Give the extent of all Plasmodium falciparum-infected red blood cells.
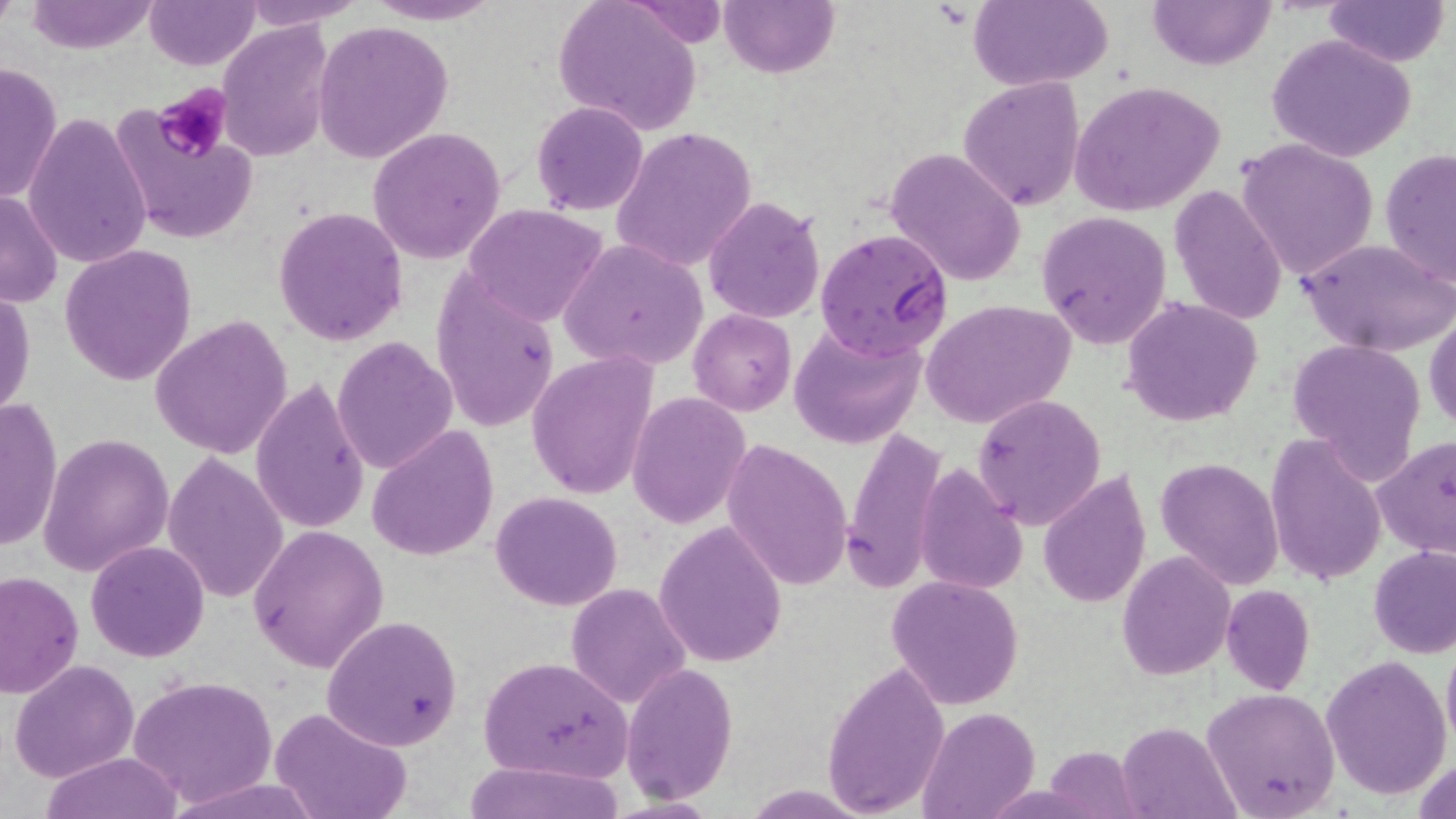

Approximate bounding boxes as (x1,y1)-(x2,y2) corner pairs in pixels.
Plasmodium falciparum-infected red blood cells: (814,227)-(953,361).

Platelet locations: (152,83)-(233,163). Uninfected red blood cell locations: (0,0)-(19,32), (23,0)-(161,54), (145,0)-(260,71), (241,0)-(368,28), (362,0)-(504,25), (553,0)-(700,135), (719,0)-(838,79), (968,0)-(1111,90), (1147,0)-(1274,71), (1325,0)-(1449,68), (218,21)-(336,162), (314,21)-(453,163), (1268,34)-(1416,163), (0,59)-(62,206), (959,77)-(1086,211), (1070,80)-(1226,218), (532,101)-(649,216), (111,105)-(260,247), (25,112)-(152,271), (610,127)-(757,271), (368,128)-(507,265), (1235,137)-(1380,281), (888,147)-(1025,286), (1380,149)-(1456,289), (1168,185)-(1289,325), (1,189)-(64,309), (703,195)-(825,324), (462,203)-(608,327), (273,207)-(408,344), (1037,211)-(1171,349), (1296,236)-(1456,358), (559,238)-(709,373), (59,245)-(197,386), (431,273)-(560,434), (1,285)-(35,421), (1121,297)-(1264,426), (924,300)-(1075,431), (688,308)-(796,416), (1426,313)-(1456,434), (150,315)-(295,458), (790,322)-(927,450), (332,335)-(458,474), (1284,339)-(1427,480), (526,352)-(657,501), (252,378)-(370,534), (627,393)-(750,527), (973,395)-(1106,529), (0,398)-(63,554), (368,424)-(497,562), (840,428)-(949,594), (37,432)-(175,577), (1265,434)-(1385,589), (1374,435)-(1456,561), (721,439)-(852,591), (162,454)-(289,604), (1156,456)-(1284,590), (913,465)-(1026,595), (1036,470)-(1152,613), (490,491)-(622,611), (653,520)-(788,667), (246,525)-(389,673), (85,540)-(210,662), (1369,545)-(1456,659), (1116,551)-(1234,679), (1,572)-(83,696), (886,575)-(1024,710), (565,582)-(690,709), (1220,583)-(1315,695), (321,615)-(461,752), (1442,635)-(1456,755), (477,655)-(632,782), (1321,655)-(1453,801), (9,658)-(139,782), (821,659)-(949,816), (622,665)-(738,803), (128,674)-(276,808), (1200,688)-(1340,816), (270,705)-(411,819), (914,707)-(1041,819), (1117,720)-(1239,818), (1042,745)-(1144,817), (40,752)-(184,819), (460,760)-(627,819). Slide-level diagnosis: Plasmodium falciparum. Thin blood smear. Light microscopy. Single field of view. Image is 1456×819 pixels. May-Grünwald-Giemsa stain. Captured at 1000x magnification.